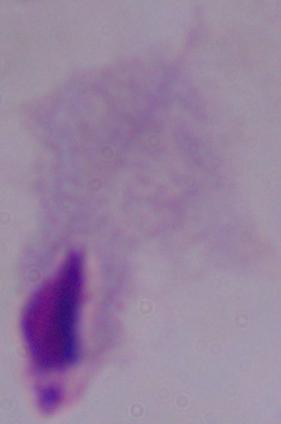
A trichomonad is seen. 1000x magnification. Micrograph.